State which parasite is depicted.
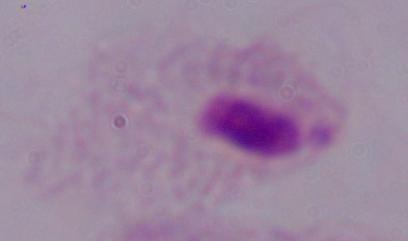

This is a trichomonad.

Captured at 1000x magnification. Micrograph.